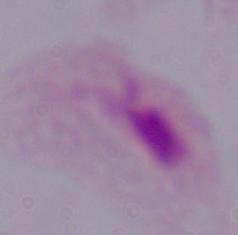
modality = micrograph
identification = trichomonad
magnification = 1000x